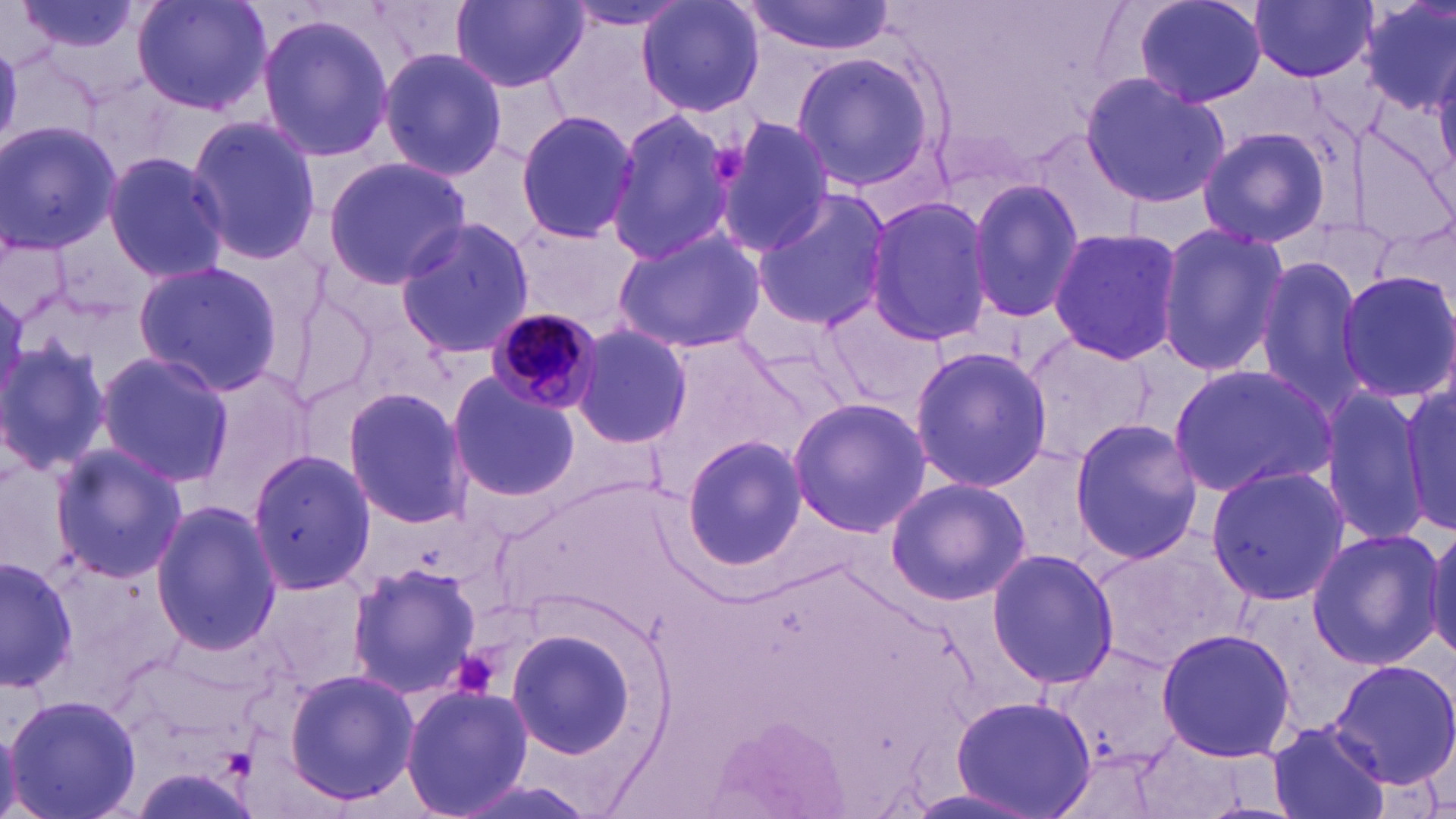

slide-level diagnosis = Plasmodium malariae
image size = 1456×819 pixels
Plasmodium malariae-infected red blood cell locations = approximate bounding boxes as (x1,y1)-(x2,y2) corner pairs in pixels: (487,306)-(603,416)
magnification = 1000x
preparation = thin blood film
modality = optical microscopy
stain = May-Grünwald-Giemsa
uninfected red blood cell locations = approximate bounding boxes as (x1,y1)-(x2,y2) corner pairs in pixels: (13,0)-(147,62), (132,0)-(271,116), (635,0)-(766,118), (1133,0)-(1268,110), (1251,0)-(1376,82), (451,1)-(586,93), (738,1)-(897,57), (1355,1)-(1456,114), (561,3)-(701,32), (255,13)-(396,163), (376,48)-(509,179), (787,49)-(941,194), (1080,72)-(1228,210), (607,108)-(736,264), (514,110)-(638,245), (187,115)-(321,268), (712,119)-(835,259), (0,122)-(122,253), (1194,124)-(1334,250), (1023,129)-(1143,242), (101,151)-(230,285), (319,156)-(472,287), (966,176)-(1086,325), (749,188)-(894,329), (864,197)-(993,347), (394,217)-(536,359), (509,222)-(644,324), (610,224)-(767,355), (1156,224)-(1288,376), (1047,228)-(1182,362), (1252,254)-(1373,419), (132,261)-(285,393), (1337,269)-(1455,403), (817,291)-(946,420), (569,323)-(693,450), (1021,333)-(1156,467), (1,335)-(113,477), (908,344)-(1053,494), (93,350)-(233,487), (1168,364)-(1337,498), (447,374)-(581,502), (1400,380)-(1454,535), (342,385)-(473,531), (1318,389)-(1430,546), (786,397)-(931,538), (1067,418)-(1204,564), (679,434)-(808,573), (47,444)-(189,582), (247,447)-(377,593), (1205,462)-(1351,606), (885,476)-(1030,606), (151,499)-(280,655), (1425,524)-(1456,665), (1304,527)-(1444,672), (1088,530)-(1248,673), (987,548)-(1119,689), (0,554)-(77,694), (345,560)-(481,700), (508,626)-(643,761), (1154,627)-(1297,761), (1326,660)-(1456,791), (283,669)-(418,805), (399,683)-(533,818), (5,693)-(143,819), (950,696)-(1097,817), (706,715)-(848,819), (1266,719)-(1393,819), (0,722)-(21,818)
platelet locations = approximate bounding boxes as (x1,y1)-(x2,y2) corner pairs in pixels: (703,144)-(749,184), (455,649)-(501,702)
field of view = single